Assess this cell for malaria.
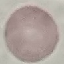

Uninfected.

{
  "image_type": "automatically extracted cell patch, resized to 64 × 64 pixels",
  "capture": "smartphone camera at the microscope eyepiece",
  "preparation": "thin blood film",
  "stain": "Giemsa"
}